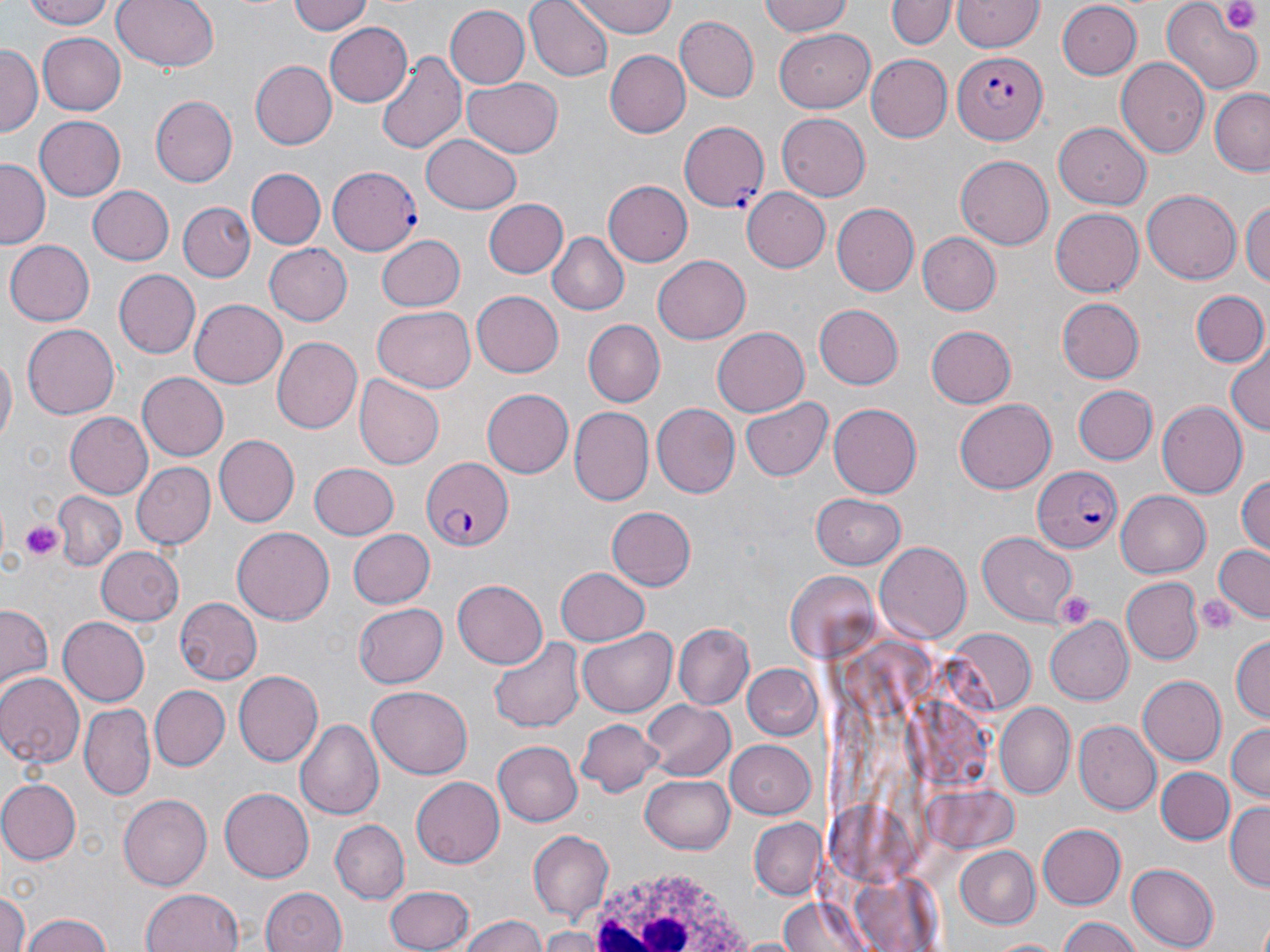
Summary:
  - Coordinate format: approximate bounding boxes as (x1, y1, x2, y2) in pixels
  - White blood cell locations: (579, 867, 757, 948)
  - Plasmodium falciparum-infected red blood cell locations: (955, 49, 1047, 146), (678, 121, 770, 213), (329, 166, 421, 255), (421, 456, 513, 550), (1029, 463, 1118, 553)
  - Platelet locations: (1226, 3, 1256, 34), (19, 519, 65, 562), (1052, 591, 1097, 629), (1196, 596, 1237, 633)
  - Uninfected red blood cell locations: (28, 0, 117, 29), (111, 0, 219, 73), (288, 0, 373, 35), (524, 0, 613, 80), (574, 0, 677, 37), (758, 0, 855, 37), (954, 0, 1045, 53), (886, 1, 952, 51), (1160, 3, 1259, 93), (1058, 4, 1142, 80), (443, 5, 528, 89), (676, 16, 759, 101), (326, 24, 413, 106), (776, 28, 878, 110), (39, 32, 127, 115), (0, 46, 39, 137), (376, 50, 466, 157), (605, 51, 690, 138), (867, 55, 952, 141), (1118, 59, 1209, 158), (248, 60, 337, 150), (464, 76, 563, 156), (1209, 91, 1269, 175), (151, 95, 237, 186), (775, 113, 871, 201), (34, 115, 126, 201), (1054, 121, 1152, 209), (422, 132, 521, 211), (956, 156, 1053, 251), (0, 159, 48, 249), (248, 168, 326, 249), (604, 181, 691, 265), (89, 187, 173, 265), (740, 187, 831, 273), (1142, 191, 1240, 283), (1241, 196, 1270, 289), (108, 198, 259, 271), (484, 199, 568, 277), (179, 202, 254, 281), (831, 202, 919, 295), (1050, 208, 1145, 298), (548, 231, 629, 316), (917, 232, 1001, 315), (376, 233, 466, 311), (4, 240, 96, 326), (263, 242, 351, 326), (654, 255, 751, 344), (113, 269, 200, 359), (471, 289, 564, 376), (1189, 289, 1270, 368), (1058, 296, 1145, 383), (190, 298, 289, 389), (814, 304, 903, 389), (373, 306, 474, 393), (583, 319, 666, 405), (24, 323, 118, 419), (926, 325, 1017, 408), (711, 327, 809, 417), (272, 335, 365, 433), (1226, 347, 1269, 438), (0, 348, 16, 450), (137, 372, 229, 460), (357, 372, 445, 468), (1072, 385, 1158, 465), (482, 388, 574, 478), (739, 396, 831, 481), (955, 400, 1057, 494), (1155, 401, 1248, 498), (829, 402, 924, 497), (651, 403, 740, 498), (569, 406, 653, 506), (64, 412, 153, 498), (215, 436, 297, 527), (309, 462, 400, 540), (131, 463, 216, 549), (1234, 471, 1270, 556), (52, 490, 127, 571), (1116, 490, 1210, 577), (810, 492, 906, 569), (607, 506, 696, 590), (232, 526, 334, 624), (345, 527, 433, 609), (979, 531, 1079, 622), (875, 543, 970, 643), (1212, 544, 1270, 623), (95, 547, 183, 627), (555, 567, 650, 647), (783, 571, 882, 662), (453, 578, 547, 669), (1122, 578, 1201, 663), (175, 597, 260, 685), (355, 603, 447, 687), (1, 604, 52, 691), (1043, 616, 1134, 705), (57, 617, 149, 706), (674, 622, 754, 709), (579, 627, 676, 715), (948, 629, 1036, 717), (1231, 633, 1269, 726), (488, 635, 586, 733), (743, 666, 824, 741), (233, 668, 323, 767), (0, 671, 83, 768), (1137, 675, 1226, 766), (367, 684, 473, 778), (151, 685, 229, 770), (644, 700, 735, 782), (80, 703, 156, 799), (996, 705, 1075, 800), (576, 717, 662, 796), (295, 718, 384, 821), (1074, 721, 1162, 815), (1227, 722, 1270, 802), (493, 738, 580, 826), (725, 739, 815, 820), (1157, 766, 1233, 844), (642, 772, 736, 854), (411, 776, 505, 869), (0, 778, 80, 865), (219, 786, 313, 882), (118, 792, 212, 889), (1225, 800, 1269, 891), (749, 817, 826, 900), (332, 820, 409, 902), (1039, 824, 1128, 910), (528, 831, 612, 921), (951, 845, 1039, 931), (1127, 864, 1218, 948), (848, 869, 946, 952), (385, 884, 476, 952), (0, 886, 27, 952), (259, 887, 347, 952), (139, 888, 249, 952), (774, 896, 880, 952), (20, 913, 119, 952), (456, 913, 550, 952), (1056, 916, 1147, 952), (539, 927, 605, 952), (985, 937, 1069, 952)
  - Slide-level diagnosis: Plasmodium falciparum
  - Modality: light microscopy
  - Preparation: thin blood film
  - Stain: May-Grünwald-Giemsa
  - Image size: 1270×952 pixels
  - Field of view: one of a larger specimen
  - Magnification: 1000x